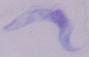
magnification = 1000x
modality = photomicrograph
identification = trypanosome